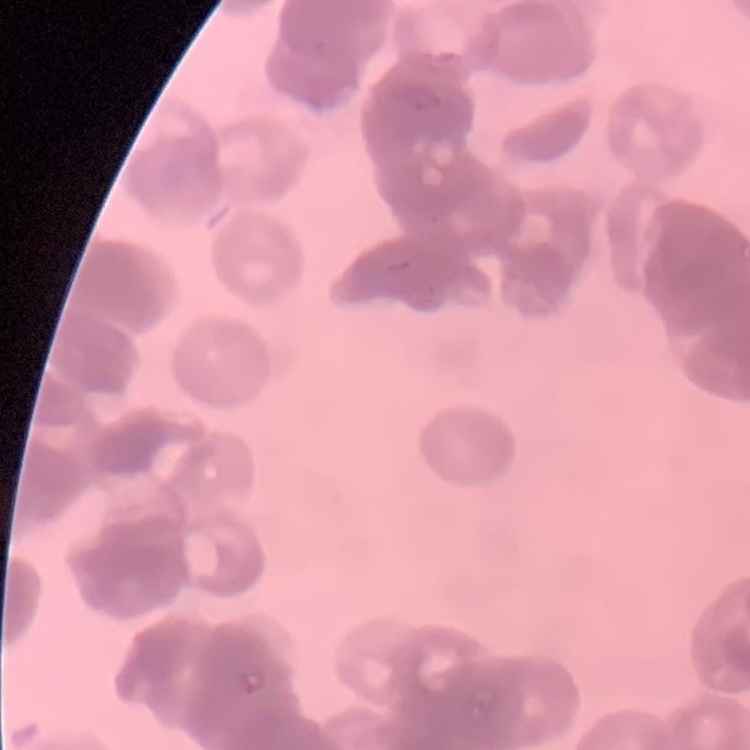
Summary:
  - Erythrocyte morphology: rouleaux formation
  - Image type: one tile cut from a larger photomicrograph
  - Stain: Field's or Giemsa
  - Preparation: thin blood smear